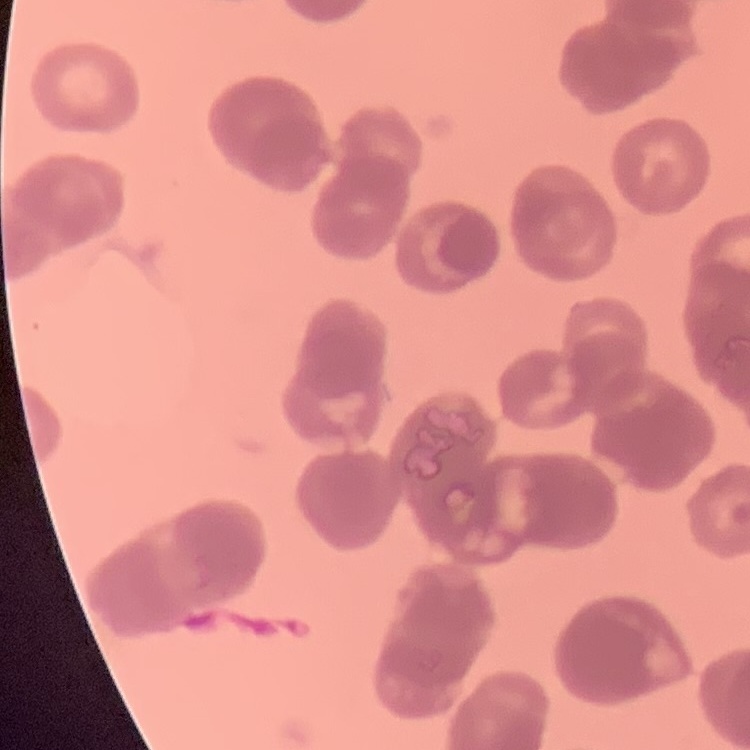
red_blood_cell_morphology: rouleaux formation
image_type: square crop of a larger photomicrograph
preparation: thin blood film
stain: Field's or Giemsa